Identify the parasite.
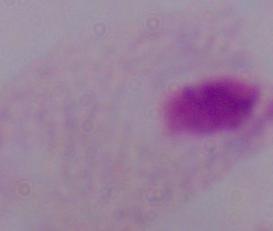
A trichomonad.

Micrograph. Captured at 1000x magnification.